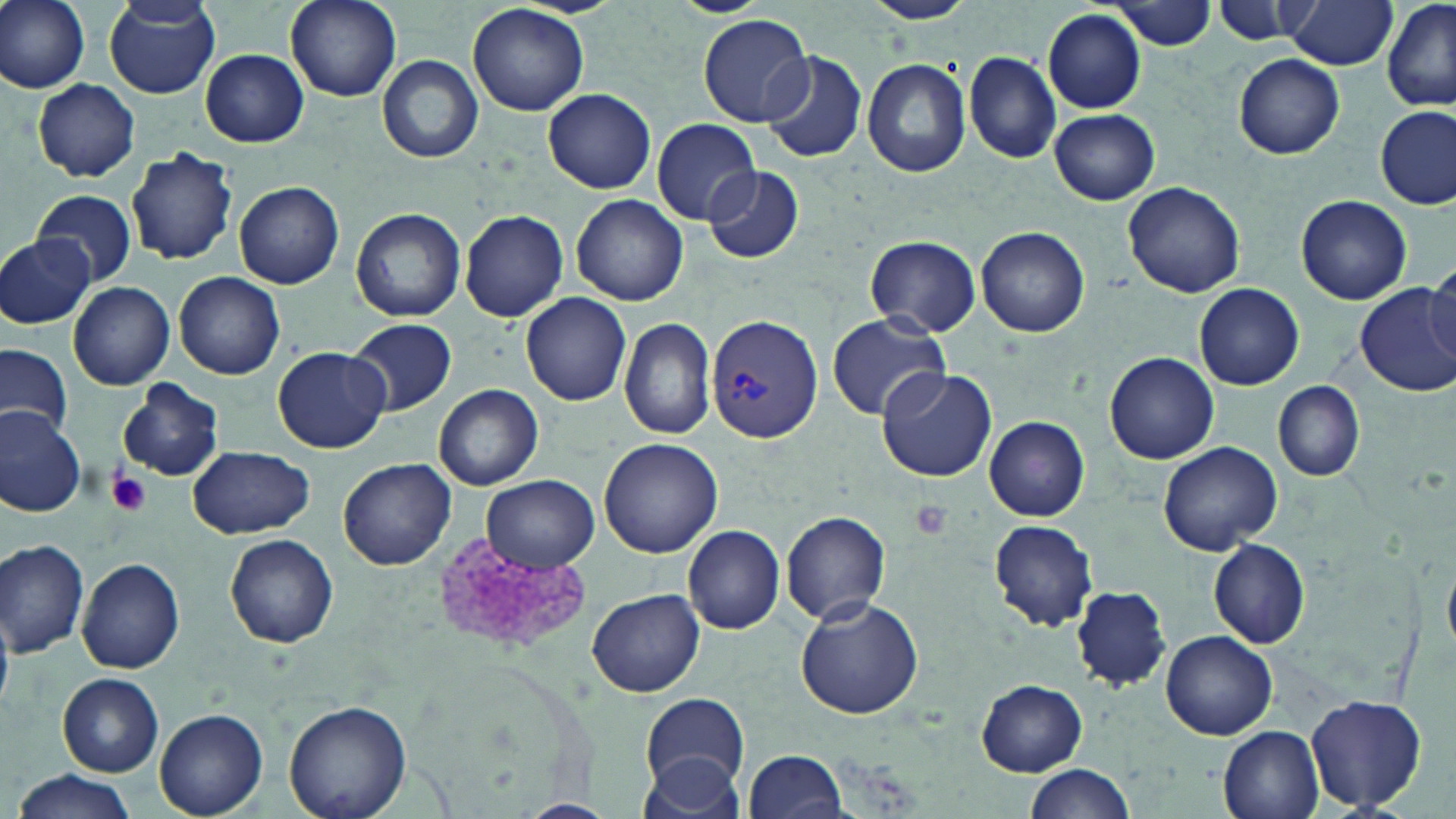
slide-level diagnosis = Plasmodium vivax
preparation = thin blood film
stain = May-Grünwald-Giemsa
magnification = 1000x
uninfected red blood cell locations = approximate bounding boxes as [x1, y1, x2, y2] in pixels: [1, 0, 92, 92], [285, 0, 402, 103], [669, 0, 770, 16], [864, 0, 978, 25], [1382, 0, 1456, 112], [1114, 1, 1216, 49], [1211, 1, 1306, 43], [1280, 1, 1396, 70], [104, 3, 221, 98], [469, 3, 589, 116], [1043, 9, 1147, 112], [698, 14, 811, 127], [200, 49, 308, 147], [760, 52, 867, 163], [964, 52, 1062, 163], [1233, 55, 1344, 159], [377, 56, 481, 163], [861, 56, 971, 178], [31, 79, 141, 180], [543, 88, 657, 194], [1375, 107, 1455, 211], [1048, 109, 1160, 204], [651, 118, 760, 224], [126, 145, 237, 266], [700, 165, 805, 265], [234, 181, 345, 289], [1122, 181, 1247, 298], [31, 187, 136, 287], [571, 194, 688, 306], [1297, 196, 1411, 305], [351, 207, 465, 322], [459, 209, 568, 321], [976, 226, 1090, 337], [0, 232, 94, 329], [865, 234, 980, 336], [1425, 265, 1456, 364], [174, 272, 286, 379], [69, 282, 175, 390], [1195, 283, 1304, 388], [1356, 284, 1456, 396], [521, 291, 632, 405], [828, 314, 951, 420], [346, 317, 457, 415], [620, 319, 717, 440], [0, 344, 74, 441], [271, 345, 391, 454], [1104, 352, 1218, 464], [876, 368, 999, 481], [118, 379, 223, 481], [1273, 382, 1363, 480], [433, 383, 544, 491], [0, 402, 85, 519], [985, 417, 1089, 521], [599, 437, 723, 558], [1158, 441, 1282, 555], [189, 443, 316, 540], [339, 458, 455, 570], [481, 476, 598, 571], [781, 510, 892, 625], [988, 519, 1098, 633], [683, 525, 785, 635], [226, 534, 339, 649], [1209, 540, 1310, 648], [1, 541, 91, 656], [76, 557, 187, 674], [1071, 585, 1175, 691], [587, 587, 705, 697], [795, 596, 925, 720], [0, 610, 14, 709], [1162, 631, 1277, 739], [59, 674, 164, 777], [976, 680, 1087, 775], [641, 693, 749, 792], [1306, 693, 1428, 813], [284, 699, 414, 819], [155, 709, 268, 818], [1218, 725, 1325, 819], [743, 749, 848, 819], [639, 754, 745, 817], [1022, 763, 1135, 819], [10, 770, 139, 819]
image size = 1456×819 pixels
platelet locations = approximate bounding boxes as [x1, y1, x2, y2] in pixels: [108, 471, 153, 517], [908, 500, 954, 542], [433, 532, 593, 654]
Plasmodium vivax-infected red blood cell locations = approximate bounding boxes as [x1, y1, x2, y2] in pixels: [707, 315, 824, 443]
field of view = single
modality = light microscopy